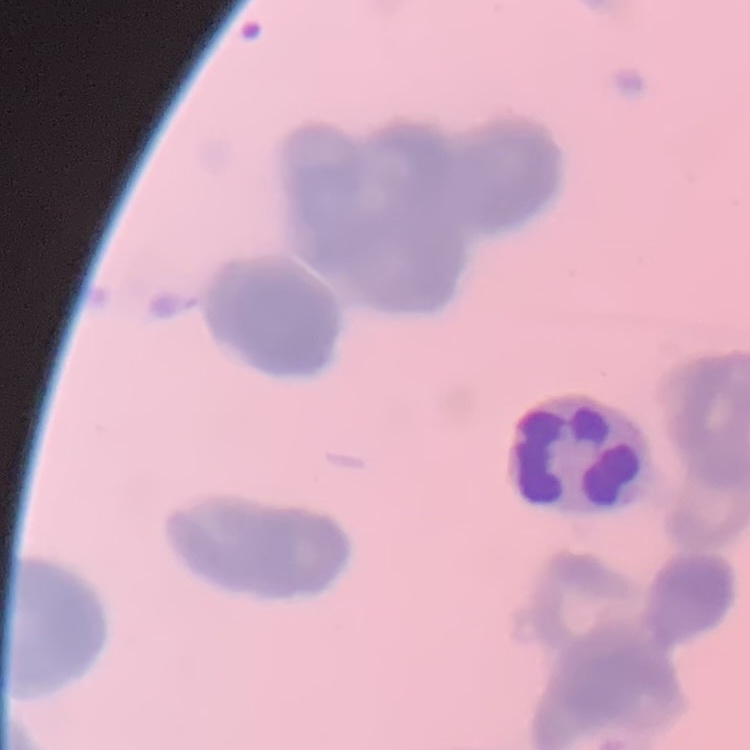 The erythrocytes show rouleaux formation. Stained with either Field's or Giemsa. Square crop of a larger photomicrograph. Thin blood film.